Locate every uninfected red blood cell.
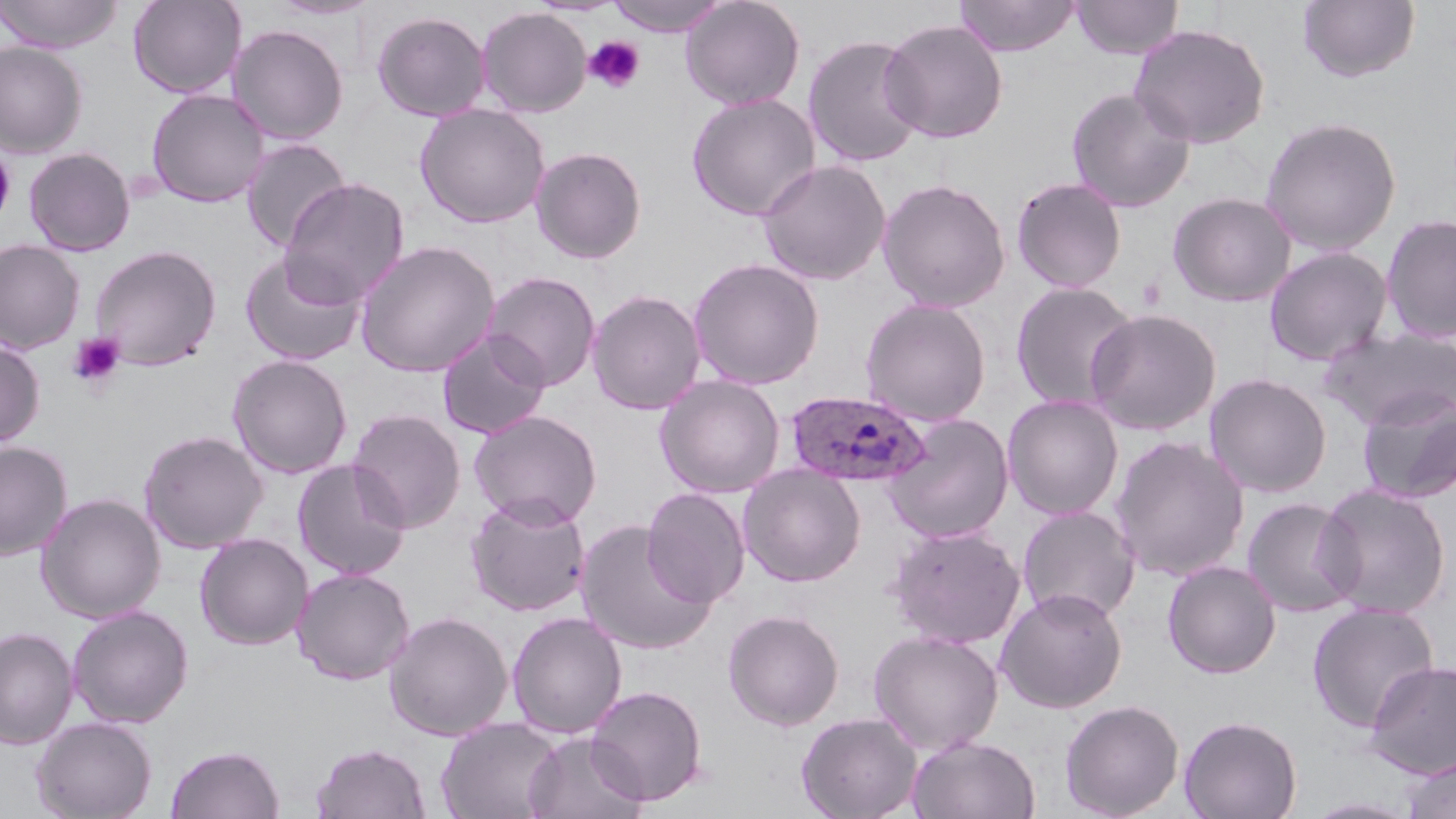

Approximate bounding boxes as named x1/y1/x2/y2 corners in pixels.
Uninfected red blood cells: (x1=0, y1=0, x2=125, y2=54), (x1=127, y1=0, x2=248, y2=99), (x1=265, y1=0, x2=381, y2=20), (x1=605, y1=0, x2=731, y2=36), (x1=679, y1=0, x2=805, y2=110), (x1=953, y1=0, x2=1082, y2=57), (x1=1070, y1=0, x2=1185, y2=60), (x1=1298, y1=0, x2=1421, y2=84), (x1=476, y1=7, x2=592, y2=117), (x1=371, y1=10, x2=491, y2=122), (x1=879, y1=19, x2=1009, y2=144), (x1=1129, y1=23, x2=1271, y2=149), (x1=227, y1=24, x2=349, y2=145), (x1=803, y1=34, x2=926, y2=168), (x1=0, y1=41, x2=88, y2=158), (x1=1066, y1=86, x2=1196, y2=212), (x1=145, y1=89, x2=269, y2=208), (x1=686, y1=93, x2=822, y2=221), (x1=414, y1=104, x2=550, y2=228), (x1=1259, y1=115, x2=1403, y2=256), (x1=240, y1=137, x2=353, y2=253), (x1=0, y1=145, x2=15, y2=229), (x1=530, y1=146, x2=647, y2=264), (x1=23, y1=147, x2=136, y2=256), (x1=757, y1=159, x2=891, y2=285), (x1=1011, y1=176, x2=1127, y2=293), (x1=278, y1=178, x2=410, y2=308), (x1=877, y1=178, x2=1011, y2=312), (x1=1167, y1=191, x2=1298, y2=307), (x1=1381, y1=213, x2=1456, y2=344), (x1=0, y1=239, x2=85, y2=354), (x1=355, y1=240, x2=500, y2=378), (x1=89, y1=244, x2=222, y2=371), (x1=1263, y1=246, x2=1393, y2=367), (x1=240, y1=250, x2=366, y2=366), (x1=688, y1=257, x2=825, y2=390), (x1=481, y1=271, x2=602, y2=391), (x1=1010, y1=281, x2=1140, y2=413), (x1=587, y1=289, x2=706, y2=415), (x1=859, y1=297, x2=992, y2=426), (x1=1084, y1=308, x2=1222, y2=436), (x1=1322, y1=327, x2=1456, y2=431), (x1=436, y1=331, x2=551, y2=439), (x1=0, y1=338, x2=46, y2=447), (x1=227, y1=353, x2=353, y2=479), (x1=1204, y1=372, x2=1332, y2=498), (x1=654, y1=374, x2=785, y2=498), (x1=1356, y1=389, x2=1456, y2=505), (x1=1002, y1=395, x2=1124, y2=520), (x1=347, y1=408, x2=467, y2=534), (x1=469, y1=409, x2=603, y2=528), (x1=883, y1=413, x2=1015, y2=544), (x1=138, y1=429, x2=268, y2=554), (x1=1110, y1=435, x2=1250, y2=582), (x1=0, y1=441, x2=72, y2=561), (x1=292, y1=459, x2=412, y2=580), (x1=738, y1=464, x2=866, y2=587), (x1=1315, y1=481, x2=1453, y2=620), (x1=641, y1=487, x2=751, y2=607), (x1=36, y1=493, x2=166, y2=623), (x1=465, y1=494, x2=591, y2=617), (x1=1241, y1=497, x2=1362, y2=617), (x1=1017, y1=505, x2=1140, y2=624), (x1=576, y1=520, x2=717, y2=655), (x1=886, y1=524, x2=1026, y2=649), (x1=195, y1=533, x2=313, y2=650), (x1=1162, y1=560, x2=1281, y2=679), (x1=292, y1=568, x2=415, y2=685), (x1=996, y1=587, x2=1128, y2=713), (x1=1306, y1=602, x2=1440, y2=733), (x1=66, y1=605, x2=194, y2=728), (x1=723, y1=609, x2=845, y2=731), (x1=384, y1=611, x2=513, y2=741), (x1=506, y1=611, x2=628, y2=739), (x1=0, y1=626, x2=78, y2=750), (x1=868, y1=629, x2=1004, y2=755), (x1=1364, y1=659, x2=1456, y2=780), (x1=586, y1=684, x2=707, y2=806), (x1=1059, y1=699, x2=1184, y2=818), (x1=796, y1=711, x2=922, y2=819), (x1=1179, y1=714, x2=1302, y2=819), (x1=31, y1=716, x2=157, y2=819), (x1=436, y1=716, x2=564, y2=819), (x1=522, y1=731, x2=648, y2=819), (x1=908, y1=735, x2=1041, y2=819), (x1=310, y1=742, x2=431, y2=819), (x1=165, y1=744, x2=284, y2=819), (x1=1400, y1=754, x2=1456, y2=819), (x1=1302, y1=797, x2=1421, y2=818).

Summary:
  - Platelet locations: (x1=584, y1=35, x2=646, y2=94), (x1=67, y1=332, x2=126, y2=390)
  - Plasmodium ovale-infected red blood cell locations: (x1=785, y1=390, x2=933, y2=489)
  - Slide-level diagnosis: Plasmodium ovale
  - Magnification: 1000x
  - Field of view: one of a larger specimen
  - Stain: May-Grünwald-Giemsa
  - Modality: optical microscopy
  - Preparation: thin blood smear
  - Image size: 1456×819 pixels